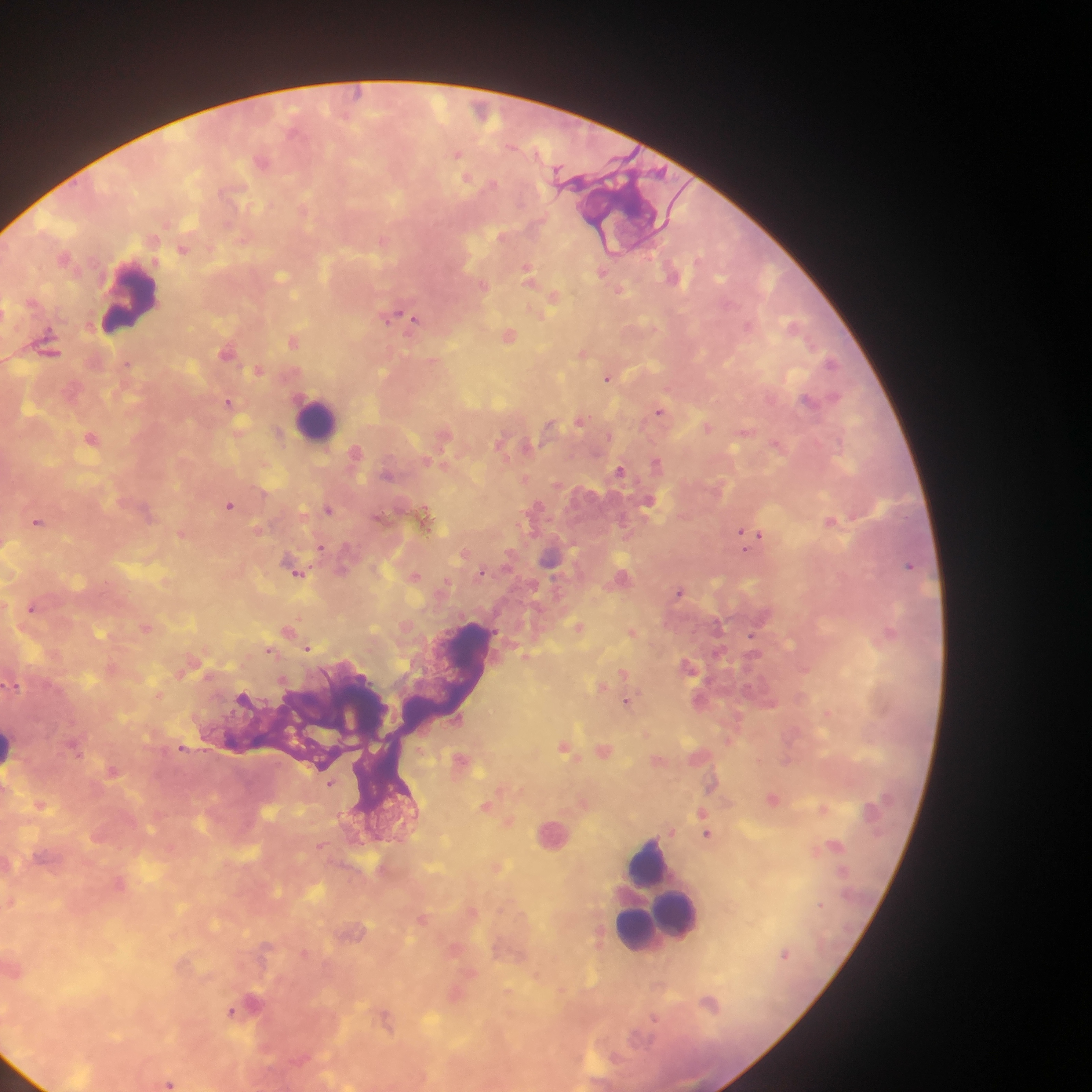
capture = mobile-phone photograph through a microscope
field of view = single
image size = 1092×1092 pixels
malaria parasite locations = approximate centers as [x, y] in pixels: [482, 111], [457, 153], [262, 160], [467, 178], [382, 239], [183, 249], [528, 269], [602, 272], [673, 275], [281, 276], [482, 285], [620, 290], [554, 296], [389, 316], [414, 319], [508, 334], [295, 340], [48, 347], [228, 351], [584, 353], [831, 362], [127, 363], [259, 369], [609, 377], [230, 402], [661, 411], [581, 420], [551, 425], [707, 426], [745, 431], [280, 433], [444, 433], [91, 437], [502, 442], [776, 443], [527, 446], [356, 451], [657, 463], [443, 464], [620, 469], [525, 479], [649, 500], [230, 505], [329, 509], [426, 518], [831, 521], [38, 522], [258, 530], [183, 533], [742, 533], [759, 536], [321, 547], [465, 552], [551, 556], [909, 565], [341, 570], [297, 571], [482, 571], [414, 576], [622, 577], [165, 581], [445, 583], [680, 591], [33, 607], [147, 626], [579, 626], [289, 630], [632, 631], [889, 633], [753, 635], [308, 648], [270, 649], [526, 656], [112, 667], [690, 667], [181, 672], [624, 672], [13, 684], [602, 686], [158, 694], [700, 700], [627, 701], [828, 712], [647, 734], [565, 746], [183, 747], [75, 748], [604, 749], [462, 760], [658, 760], [113, 771], [331, 783], [713, 784], [773, 798], [40, 804], [487, 805], [823, 808], [703, 812], [509, 821], [671, 830], [707, 833], [835, 845], [321, 846], [496, 866], [119, 883], [11, 901], [472, 911], [423, 918], [599, 936], [455, 948], [786, 952], [305, 953], [562, 990], [455, 993], [710, 1003], [245, 1006], [232, 1012], [386, 1018], [169, 1082]
preparation = thick blood film
country = Ghana
leukocyte locations = approximate centers as [x, y] in pixels: [129, 297], [319, 419], [10, 750], [552, 834], [651, 870], [678, 912], [661, 914]